Point out every Plasmodium parasite and every leukocyte.
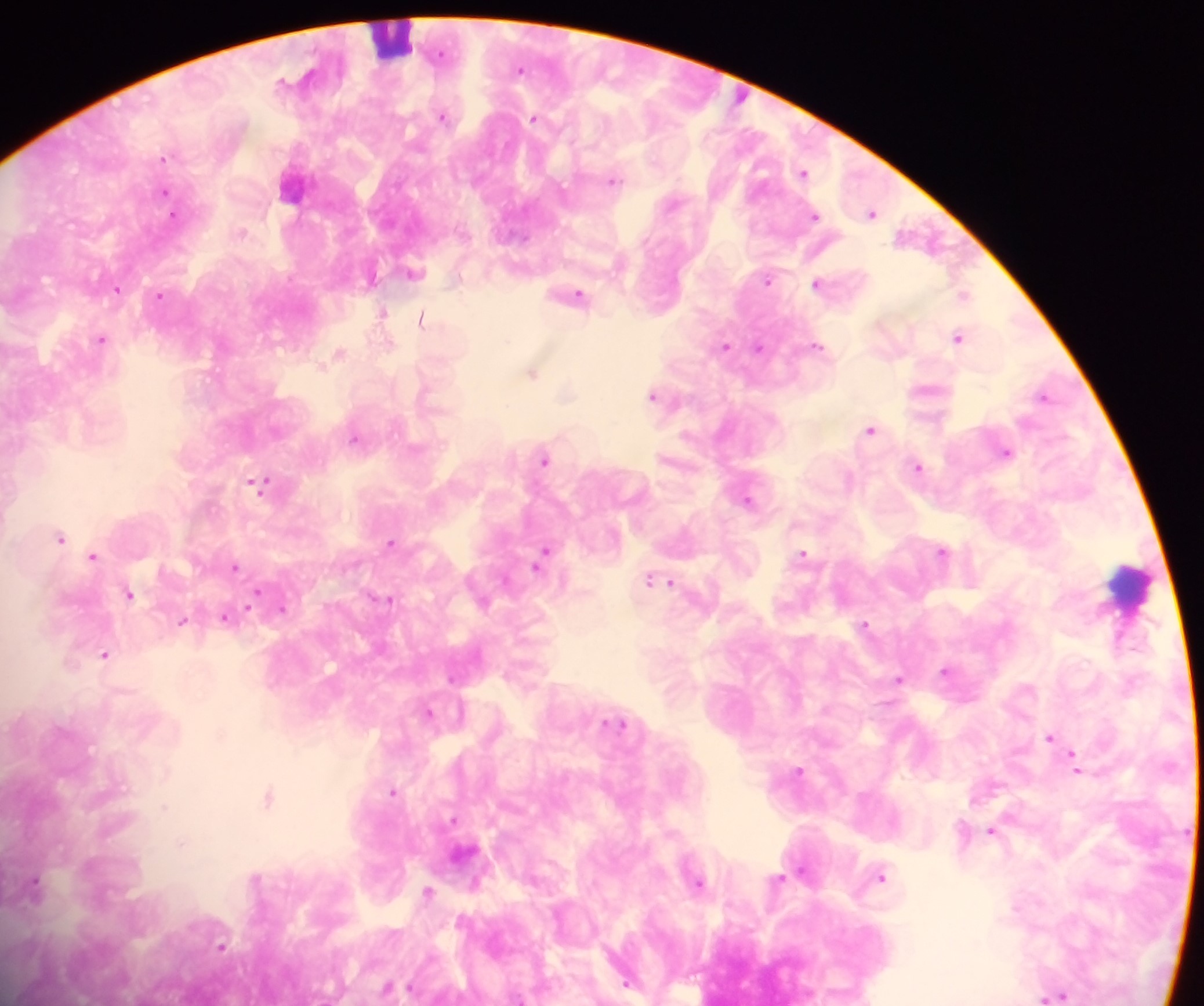
Approximate centers as {x, y} in pixels.
Plasmodium parasites: {520, 68}, {443, 115}, {534, 117}, {164, 156}, {803, 171}, {613, 178}, {165, 191}, {872, 212}, {173, 214}, {815, 215}, {242, 231}, {414, 272}, {371, 278}, {768, 278}, {817, 282}, {117, 289}, {578, 294}, {964, 294}, {160, 295}, {383, 312}, {422, 318}, {958, 336}, {101, 338}, {390, 341}, {725, 344}, {817, 345}, {759, 346}, {339, 351}, {532, 371}, {567, 392}, {653, 394}, {1044, 395}, {871, 429}, {354, 438}, {1006, 451}, {545, 459}, {917, 466}, {849, 479}, {260, 481}, {747, 500}, {60, 536}, {391, 542}, {942, 551}, {803, 552}, {94, 556}, {542, 556}, {235, 565}, {665, 580}, {129, 593}, {254, 596}, {386, 598}, {282, 607}, {227, 617}, {183, 620}, {865, 623}, {104, 654}, {945, 670}, {899, 678}, {429, 711}, {618, 723}, {1050, 736}, {1075, 761}, {799, 770}, {393, 791}, {270, 796}, {165, 807}, {992, 830}, {881, 876}, {779, 878}, {699, 881}, {476, 883}, {35, 885}, {429, 892}, {221, 945}, {628, 984}, {389, 988}, {1057, 995}.
Leukocytes: {392, 37}, {1130, 586}.

Image is 1204×1006 pixels. Single field of view. Sample from Ghana. Thick blood film. Photographed through a microscope with a mobile-phone camera.